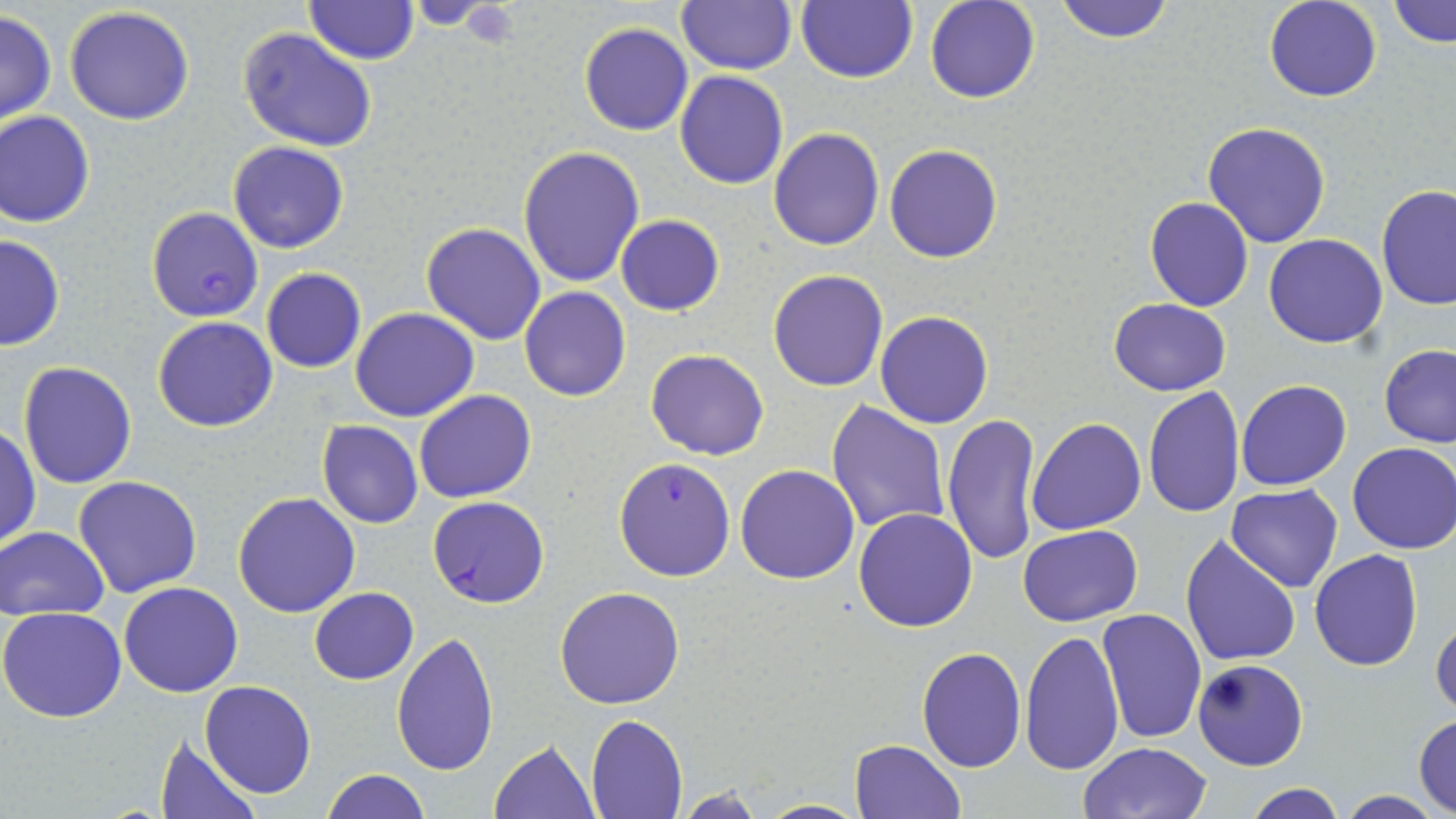
Summary:
  - Coordinate format: approximate bounding boxes as named x1/y1/x2/y2 corners in pixels
  - Platelet locations: (x1=457, y1=2, x2=521, y2=45)
  - Plasmodium falciparum-infected red blood cell locations: (x1=146, y1=206, x2=264, y2=321), (x1=427, y1=494, x2=548, y2=606)
  - Uninfected red blood cell locations: (x1=304, y1=0, x2=417, y2=65), (x1=925, y1=0, x2=1039, y2=104), (x1=1052, y1=0, x2=1176, y2=44), (x1=1263, y1=0, x2=1382, y2=102), (x1=1388, y1=0, x2=1454, y2=48), (x1=677, y1=1, x2=797, y2=75), (x1=795, y1=1, x2=918, y2=85), (x1=64, y1=5, x2=196, y2=126), (x1=0, y1=10, x2=56, y2=127), (x1=579, y1=23, x2=693, y2=136), (x1=239, y1=27, x2=377, y2=151), (x1=675, y1=71, x2=788, y2=189), (x1=0, y1=111, x2=95, y2=228), (x1=1202, y1=121, x2=1332, y2=248), (x1=769, y1=128, x2=885, y2=250), (x1=228, y1=140, x2=349, y2=254), (x1=884, y1=144, x2=1002, y2=263), (x1=517, y1=146, x2=646, y2=289), (x1=1377, y1=185, x2=1456, y2=313), (x1=1144, y1=197, x2=1253, y2=312), (x1=616, y1=214, x2=724, y2=315), (x1=421, y1=222, x2=547, y2=346), (x1=0, y1=232, x2=64, y2=352), (x1=1265, y1=233, x2=1386, y2=348), (x1=261, y1=267, x2=366, y2=373), (x1=767, y1=269, x2=889, y2=392), (x1=520, y1=286, x2=632, y2=402), (x1=1108, y1=297, x2=1232, y2=396), (x1=351, y1=307, x2=478, y2=421), (x1=876, y1=311, x2=993, y2=428), (x1=153, y1=317, x2=278, y2=433), (x1=1378, y1=344, x2=1456, y2=448), (x1=645, y1=349, x2=769, y2=460), (x1=17, y1=360, x2=138, y2=488), (x1=1236, y1=380, x2=1352, y2=492), (x1=1143, y1=387, x2=1245, y2=518), (x1=413, y1=389, x2=536, y2=503), (x1=826, y1=401, x2=950, y2=536), (x1=1044, y1=403, x2=1246, y2=526), (x1=941, y1=412, x2=1043, y2=566), (x1=1026, y1=418, x2=1145, y2=536), (x1=317, y1=420, x2=424, y2=529), (x1=0, y1=426, x2=39, y2=550), (x1=1348, y1=441, x2=1456, y2=555), (x1=615, y1=456, x2=736, y2=580), (x1=734, y1=463, x2=861, y2=584), (x1=74, y1=475, x2=204, y2=597), (x1=1226, y1=484, x2=1343, y2=592), (x1=232, y1=492, x2=361, y2=618), (x1=853, y1=508, x2=978, y2=630), (x1=1018, y1=524, x2=1143, y2=626), (x1=1, y1=525, x2=110, y2=621), (x1=1180, y1=534, x2=1303, y2=667), (x1=1309, y1=549, x2=1424, y2=672), (x1=118, y1=583, x2=244, y2=698), (x1=555, y1=586, x2=684, y2=709), (x1=310, y1=587, x2=418, y2=684), (x1=1, y1=607, x2=127, y2=723), (x1=1096, y1=608, x2=1208, y2=744), (x1=1431, y1=612, x2=1455, y2=718), (x1=1021, y1=628, x2=1125, y2=776), (x1=392, y1=632, x2=498, y2=777), (x1=915, y1=646, x2=1026, y2=772), (x1=1192, y1=659, x2=1309, y2=770), (x1=200, y1=680, x2=316, y2=799), (x1=1414, y1=713, x2=1456, y2=815), (x1=585, y1=715, x2=688, y2=819), (x1=154, y1=735, x2=260, y2=818), (x1=489, y1=739, x2=598, y2=818), (x1=848, y1=739, x2=965, y2=819), (x1=1078, y1=742, x2=1210, y2=819), (x1=321, y1=769, x2=431, y2=819), (x1=1241, y1=782, x2=1347, y2=819), (x1=672, y1=787, x2=773, y2=818), (x1=1337, y1=791, x2=1442, y2=819), (x1=754, y1=798, x2=872, y2=818)
  - Slide-level diagnosis: Plasmodium falciparum
  - Magnification: 1000x
  - Preparation: thin blood smear
  - Stain: May-Grünwald-Giemsa
  - Modality: optical microscopy
  - Image size: 1456×819 pixels
  - Field of view: one of a larger specimen